Point out each malaria parasite and each leukocyte.
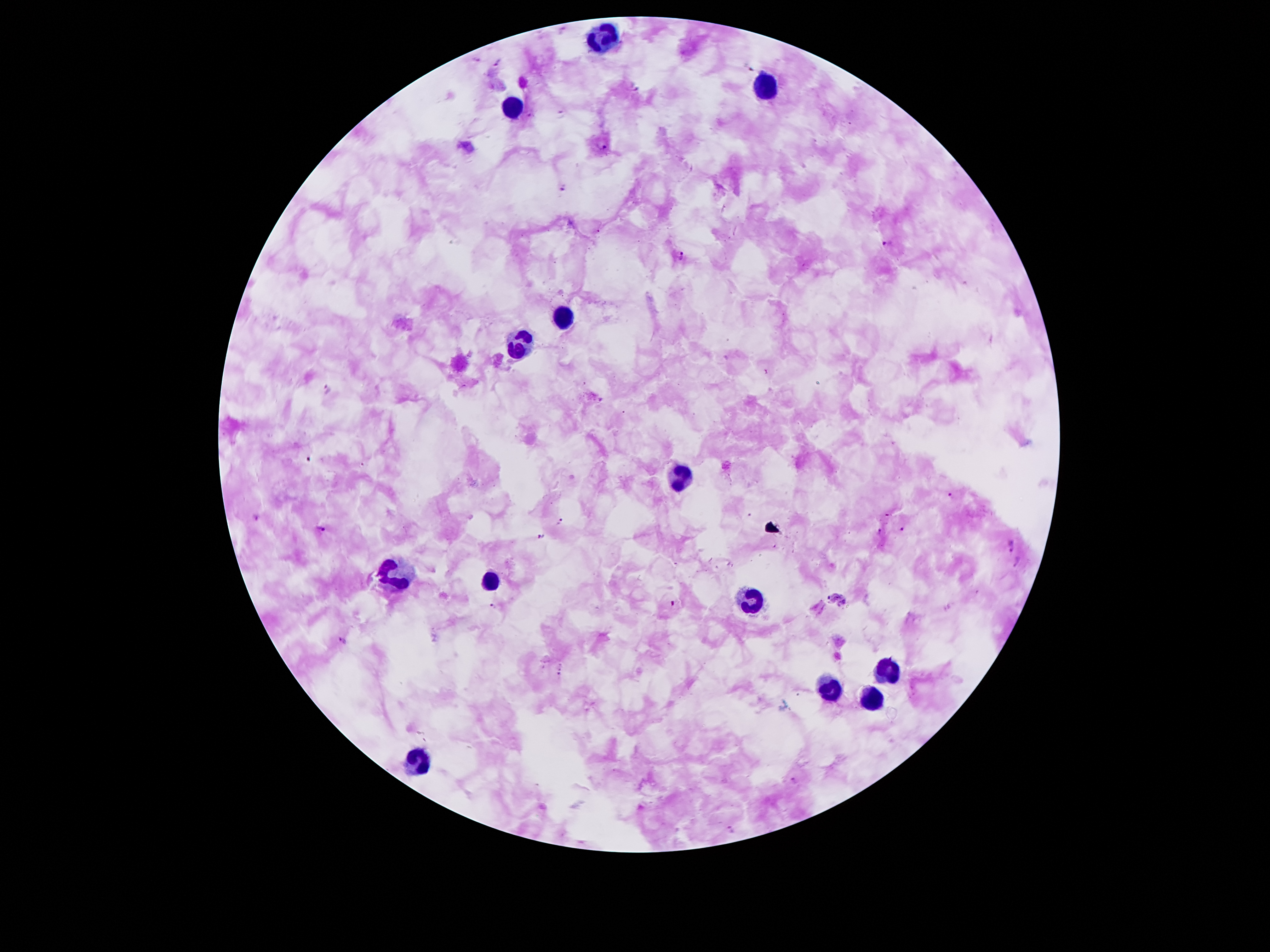
Approximate centers as (x, y) in pixels.
Malaria parasites: (497, 61), (751, 67), (636, 89), (562, 112), (602, 145), (564, 187), (887, 243), (681, 255), (328, 388), (952, 496), (258, 519), (560, 521), (902, 527), (322, 529), (880, 530), (541, 536), (1013, 547), (1018, 561), (493, 606), (344, 640), (793, 780), (731, 829).
Leukocytes: (605, 38), (762, 85), (512, 110), (568, 315), (520, 343), (683, 475), (397, 576), (490, 581), (751, 601), (883, 670), (830, 689), (871, 701), (419, 764).

capture = smartphone through the microscope eyepiece
stain = Giemsa
magnification = 100x
image size = 1270×952 pixels
field of view = single
preparation = thick peripheral-blood smear
patient malaria status = positive for Plasmodium falciparum